Report the malaria status of this cell.
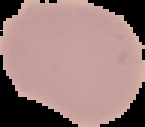
It is uninfected.

preparation = thin blood film
image type = segmented cell region with the area outside set to black
image size = 145×127 pixels